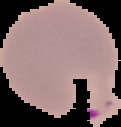
Summary:
  - Image type: segmented cell region on a black background
  - Image size: 121×127 pixels
  - Malaria status: parasitized
  - Preparation: thin blood smear